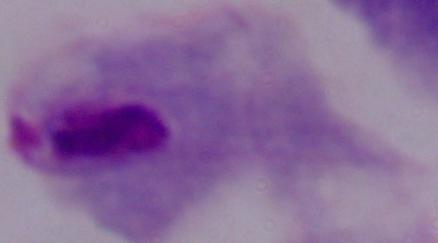

magnification: 1000x
modality: photomicrograph
identification: trichomonad